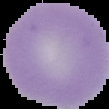

Image is 109×109 pixels. From a thin blood film. Segmented cell region on a black background. Result: negative for malaria parasites.